Give the extent of all Plasmodium ovale-infected red blood cells.
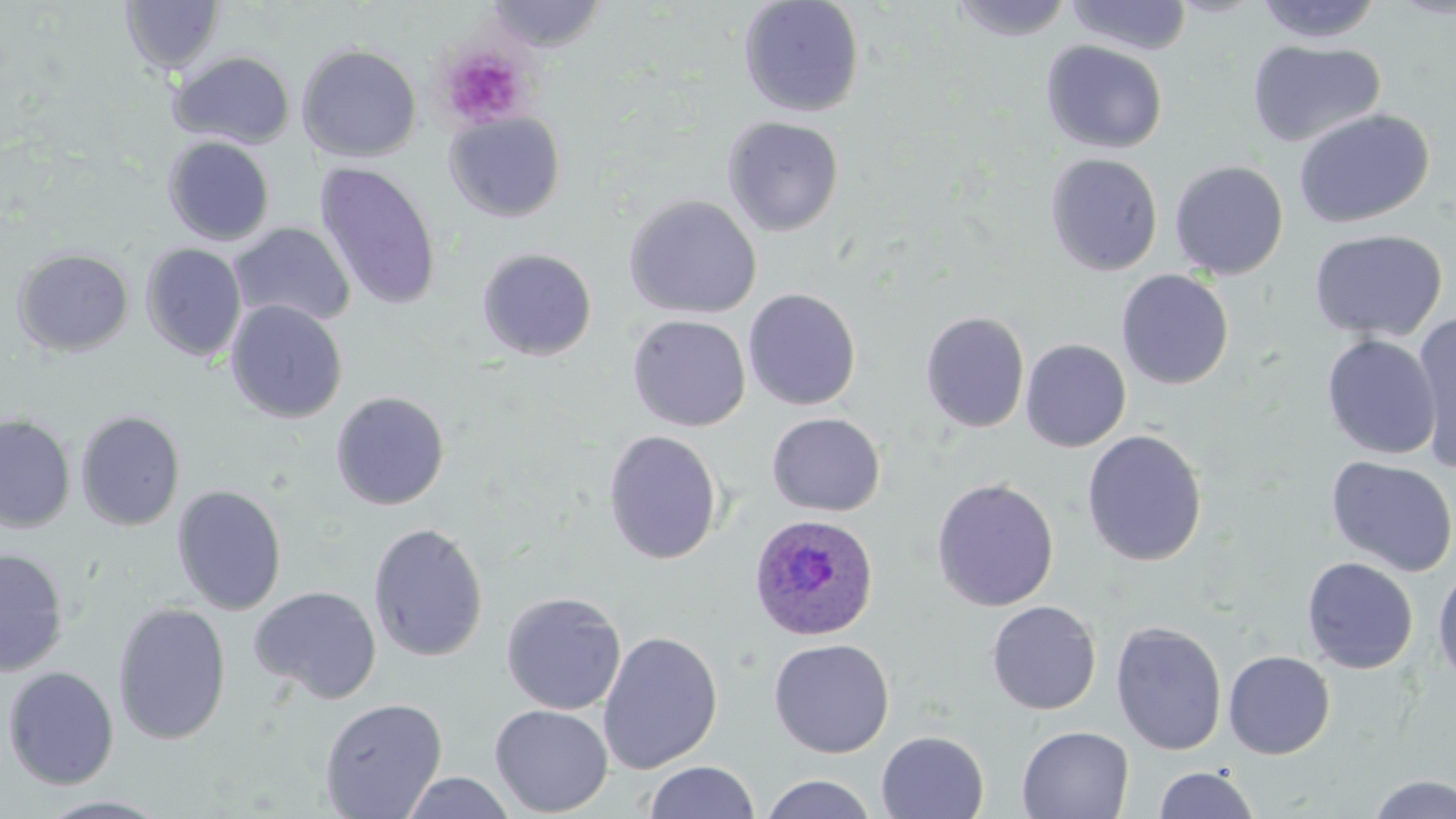

Approximate bounding boxes as [x1, y1, x2, y2] in pixels.
Plasmodium ovale-infected red blood cells: [748, 513, 879, 642].

Uninfected red blood cell locations: [738, 0, 865, 118], [947, 0, 1076, 42], [1065, 0, 1193, 56], [120, 1, 224, 76], [483, 1, 608, 52], [1254, 1, 1384, 44], [1246, 39, 1386, 149], [1041, 41, 1168, 154], [296, 43, 422, 162], [169, 50, 296, 149], [1293, 108, 1434, 228], [443, 111, 567, 223], [722, 115, 845, 237], [163, 135, 276, 246], [1044, 153, 1163, 276], [1169, 160, 1289, 280], [314, 162, 442, 310], [623, 194, 762, 319], [229, 222, 356, 329], [1309, 228, 1448, 342], [140, 243, 247, 362], [477, 247, 598, 361], [12, 248, 134, 357], [1116, 270, 1234, 390], [742, 287, 862, 411], [225, 299, 348, 424], [920, 311, 1030, 433], [1410, 312, 1456, 472], [627, 314, 751, 432], [1320, 334, 1441, 460], [1020, 338, 1132, 452], [330, 391, 450, 510], [75, 409, 186, 531], [766, 412, 885, 516], [0, 414, 76, 533], [602, 429, 723, 564], [1081, 429, 1208, 566], [1325, 455, 1456, 578], [931, 477, 1059, 612], [172, 484, 287, 615], [368, 521, 489, 663], [0, 548, 69, 676], [1301, 556, 1419, 674], [1432, 564, 1456, 690], [249, 585, 382, 704], [501, 591, 627, 715], [986, 600, 1102, 715], [112, 601, 232, 746], [1110, 621, 1227, 756], [598, 631, 723, 774], [768, 637, 895, 758], [1223, 650, 1336, 759], [2, 666, 119, 789], [319, 697, 448, 818], [489, 703, 613, 817], [1016, 725, 1135, 818], [876, 730, 990, 819], [644, 761, 760, 818], [1153, 765, 1261, 819], [400, 771, 517, 818], [1365, 773, 1456, 818], [760, 774, 878, 819], [35, 795, 173, 818]. Platelet locations: [438, 44, 534, 129]. Slide-level diagnosis: Plasmodium ovale. Captured at 1000x magnification. Image is 1456×819 pixels. Optical microscopy. One field of a larger specimen. Thin blood smear. May-Grünwald-Giemsa stain.